Assess this cell for malaria.
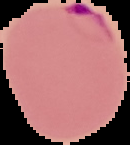
It is parasitized.

image_type: cell region segmented out of the field of view; surrounding area masked to black
image_size: 130×145 pixels
preparation: thin blood smear